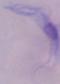
1000x magnification. Micrograph. A trypanosome is shown.